Locate every Plasmodium parasite.
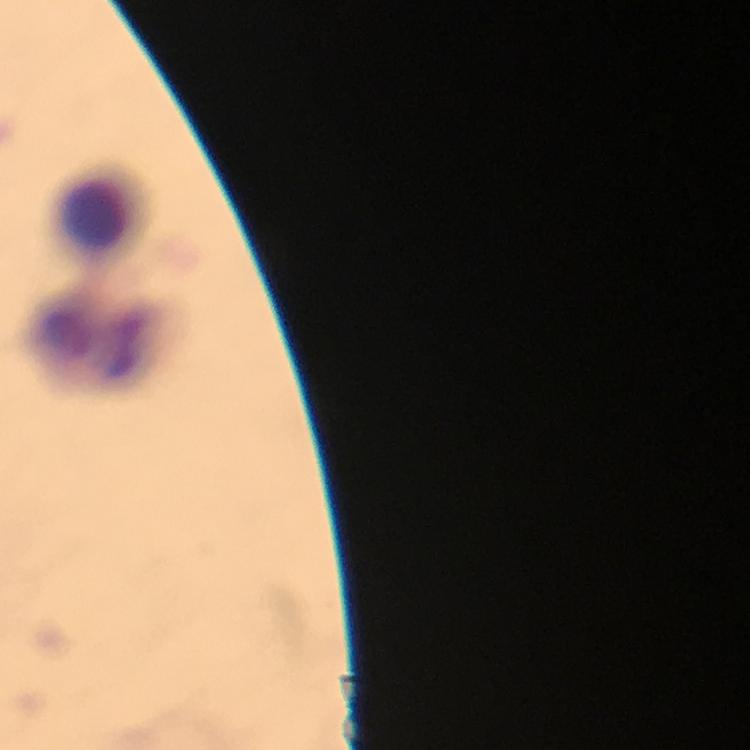
No Plasmodium parasites seen.

Approximate centers as {x, y} in pixels.
Summary:
  - Leukocyte locations: {99, 217}, {95, 339}
  - Stain: Giemsa
  - Immersion oil: applied
  - Preparation: thick blood smear
  - Context: from a malaria diagnostic workup
  - Capture: smartphone camera through the microscope
  - Image size: 750×750 pixels
  - Cropped from: a single field of view
  - Magnification: 100x